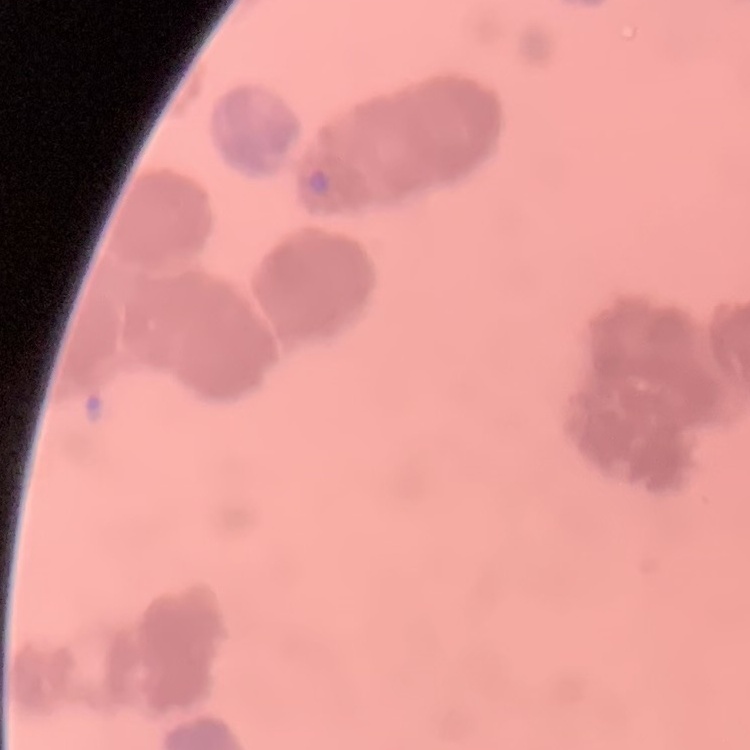

{
  "erythrocyte_morphology": "rouleaux formation",
  "stain": "Field's or Giemsa",
  "image_type": "one tile cut from a larger photomicrograph",
  "preparation": "thin peripheral smear"
}